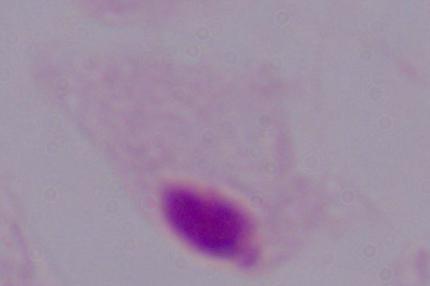

Summary:
  - Modality: photomicrograph
  - Magnification: 1000x
  - Identification: trichomonad